Find each parasitized RBC.
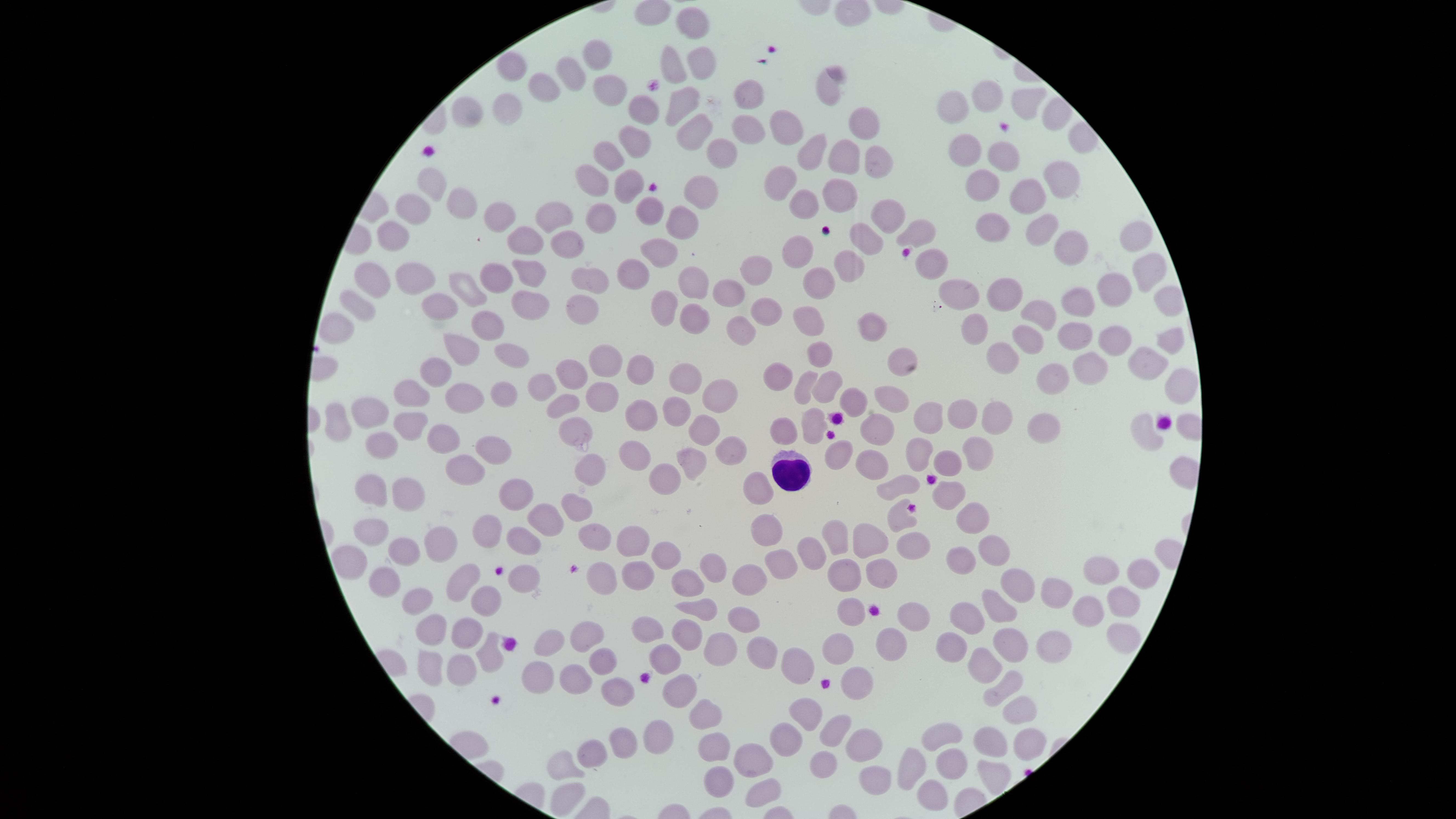

No parasitized RBCs identified.

Approximate marker points as [x, y] in pixels. Uninfected RBCs: [691, 24], [598, 54], [693, 62], [514, 68], [671, 68], [572, 75], [547, 86], [830, 87], [609, 88], [747, 95], [992, 97], [1021, 103], [680, 104], [509, 108], [959, 109], [467, 110], [642, 113], [1049, 118], [690, 129], [786, 130], [862, 130], [748, 132], [636, 142], [963, 147], [716, 148], [611, 151], [811, 152], [1004, 157], [840, 160], [879, 160], [592, 176], [433, 180], [1057, 180], [780, 182], [628, 188], [984, 188], [837, 193], [698, 195], [1030, 196], [459, 201], [802, 202], [410, 211], [497, 212], [599, 213], [647, 214], [549, 215], [682, 216], [897, 217], [1036, 226], [988, 227], [394, 235], [922, 235], [873, 238], [563, 239], [1137, 239], [530, 242], [1068, 250], [799, 251], [661, 252], [858, 263], [930, 265], [755, 268], [1141, 269], [632, 270], [506, 271], [538, 273], [412, 275], [695, 278], [587, 280], [824, 280], [374, 283], [462, 285], [963, 288], [1112, 288], [1006, 293], [726, 294], [530, 300], [1080, 301], [579, 303], [361, 307], [772, 308], [665, 309], [439, 310], [1041, 310], [692, 321], [804, 324], [334, 326], [877, 330], [486, 331], [741, 331], [971, 332], [1027, 334], [1110, 335], [1074, 336], [1169, 339], [463, 342], [821, 351], [512, 354], [1006, 356], [599, 359], [1150, 363], [897, 364], [636, 367], [1090, 370], [437, 372], [572, 373], [677, 373], [775, 375], [1054, 378], [1172, 383], [803, 384], [825, 385], [544, 388], [710, 388], [416, 391], [502, 391], [468, 397], [603, 397], [884, 397], [565, 398], [853, 399], [665, 410], [372, 412], [966, 416], [634, 417], [999, 417], [933, 419], [410, 421], [336, 424], [813, 425], [703, 427], [571, 428], [878, 429], [1045, 430], [784, 431], [442, 436], [1147, 436], [381, 445], [492, 448], [920, 449], [738, 452], [975, 453], [839, 454], [637, 459], [873, 459], [692, 460], [944, 460], [463, 474], [592, 474], [665, 478], [901, 487], [756, 488], [375, 493], [951, 493], [410, 495], [521, 495], [580, 506], [901, 514], [968, 516], [546, 517], [766, 524], [492, 528], [371, 529], [595, 530], [829, 538], [434, 542], [633, 542], [912, 542], [860, 543], [523, 544], [993, 547], [400, 553], [811, 553], [665, 557], [354, 560], [779, 561], [960, 561], [716, 567], [1101, 571], [1147, 572], [636, 573], [884, 573], [604, 577], [523, 578], [850, 579], [464, 582], [751, 582], [380, 584], [1023, 584], [687, 586], [1053, 594], [1119, 599], [1002, 605], [411, 606], [484, 606], [914, 610], [851, 612], [696, 613], [971, 616], [1086, 616], [742, 621], [435, 627], [470, 630], [647, 631], [593, 632], [1117, 635], [689, 636], [891, 640], [955, 640], [1014, 641], [547, 645], [1051, 645], [840, 647], [494, 649], [758, 650], [717, 651], [604, 659], [988, 661], [669, 662], [428, 667], [457, 671], [793, 672], [569, 683], [535, 685], [859, 685], [1004, 686], [682, 689], [619, 694], [1016, 710], [813, 711], [703, 717], [831, 732], [657, 738], [943, 740], [795, 743], [1025, 743], [623, 744], [993, 744], [864, 746], [712, 752], [593, 756], [907, 762], [757, 763], [819, 766], [564, 770], [948, 770], [993, 773], [717, 776], [880, 776], [567, 793], [764, 794], [926, 797]. WBCs: [790, 474]. Giemsa stain. Photographed with a smartphone camera through the microscope eyepiece. Image is 1456×819 pixels. Thin smear of blood. The visible region is circular. Single field of view.